State which cell type is depicted.
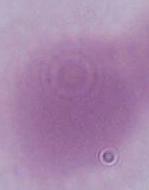

An erythrocyte.

{
  "modality": "photomicrograph",
  "magnification": "1000x"
}